Locate every Plasmodium parasite.
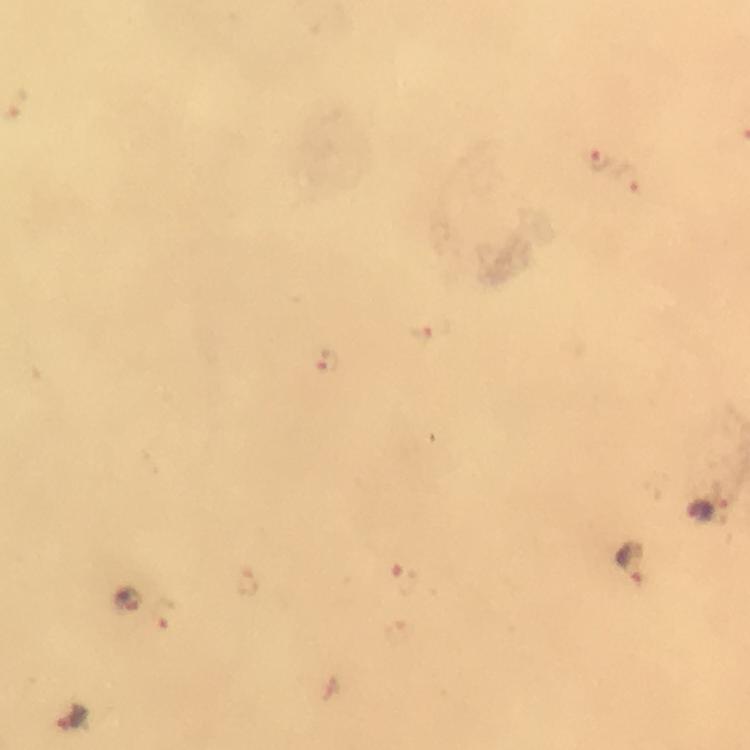
Approximate centers as (x, y) in pixels.
Plasmodium parasites: (597, 159), (629, 176), (435, 333), (328, 363), (701, 513), (634, 564), (406, 580), (247, 583), (125, 600), (164, 616), (73, 718).

Image is 750×750 pixels. 100x magnification. Cropped region of a single field of view. Immersion oil applied. Smartphone photograph taken through a microscope. Giemsa stain. Thick smear. From a malaria diagnostic workup.